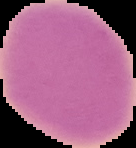 Malaria status: uninfected. The area outside the segmented cell region is set to black. From a thin blood film. Image is 136×148 pixels.